Name the cell type shown.
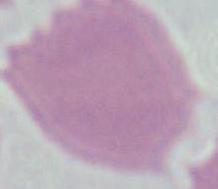

This is an erythrocyte.

{
  "modality": "micrograph",
  "magnification": "1000x"
}